Give the position of every malaria parasite.
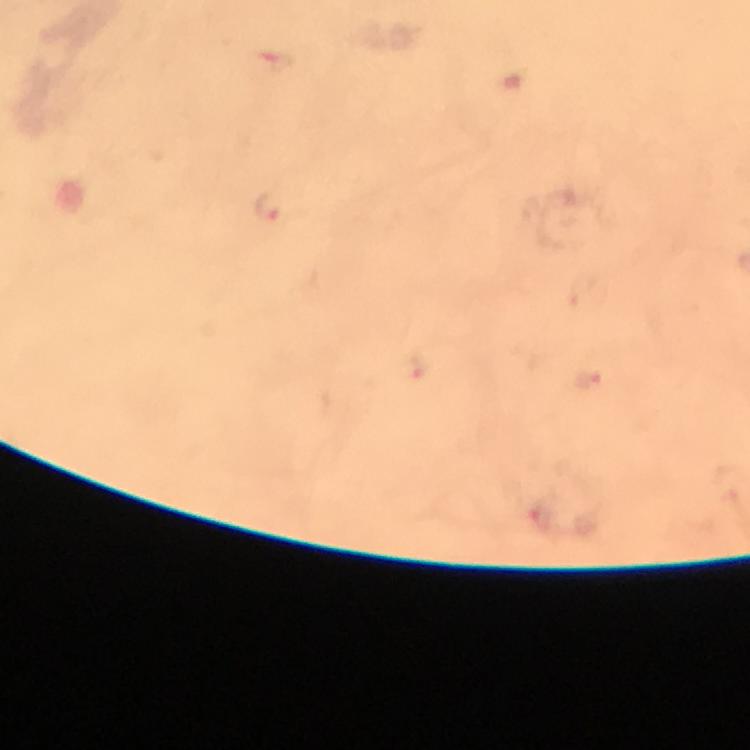

Approximate centers as {x, y} in pixels.
Malaria parasites: {267, 204}, {586, 380}.

Summary:
  - Cropped from: one field of view
  - Stain: Giemsa
  - Capture: smartphone camera through the microscope
  - Magnification: 100x
  - Immersion oil: used
  - Image size: 750×750 pixels
  - Context: from a diagnostic examination for malaria
  - Preparation: thick blood film